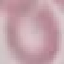 Result: negative for malaria parasites. Giemsa-stained preparation. Thin blood smear. Automatically extracted cell patch, resized to 64 × 64 pixels. Photographed with a smartphone camera at the microscope eyepiece.